Identify the parasite.
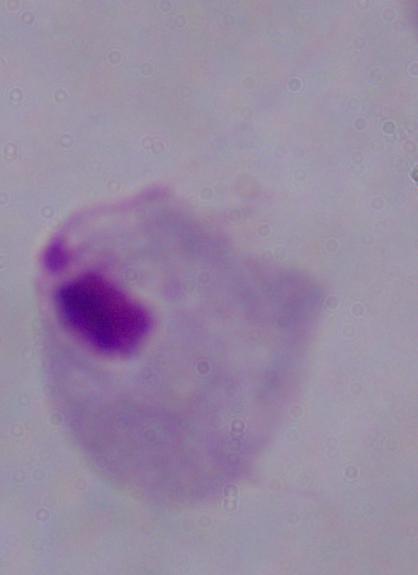
A trichomonad.

Micrograph. 1000x magnification.